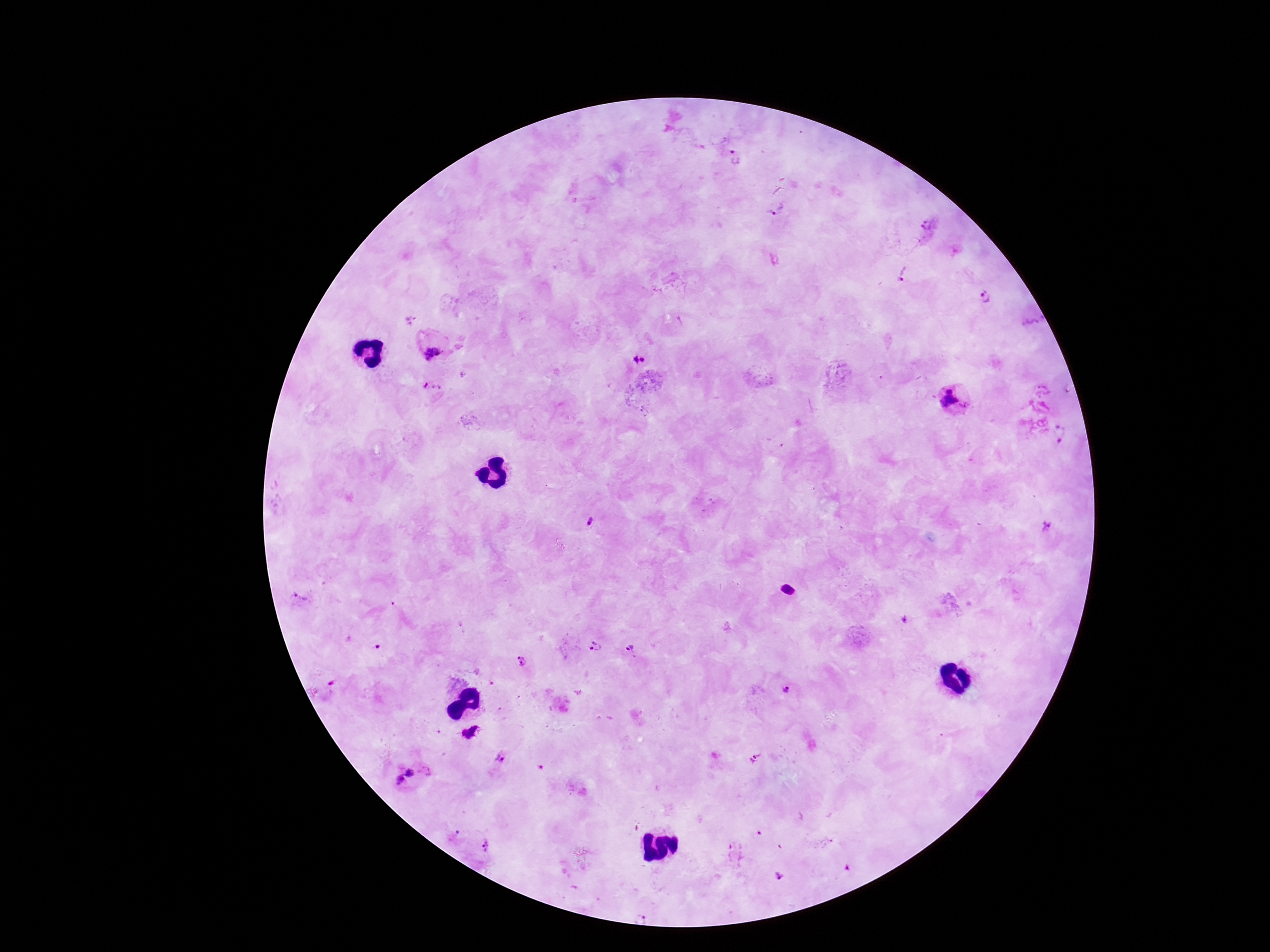
patient malaria status = positive
magnification = 100x
stain = Giemsa
capture = smartphone camera through the microscope eyepiece
field of view = one from this slide
preparation = thick peripheral-blood smear
image size = 1270×952 pixels
Plasmodium parasite locations = approximate centers as [x, y] in pixels: [735, 157], [777, 210], [929, 226], [903, 274], [984, 297], [407, 317], [431, 348], [636, 358], [434, 388], [1043, 390], [955, 405], [1060, 432], [589, 522], [1049, 525], [789, 590], [301, 598], [595, 645], [631, 649], [522, 663], [787, 689], [470, 733], [501, 760], [755, 762], [411, 780], [484, 846], [779, 878], [644, 912]